Name the parasite shown.
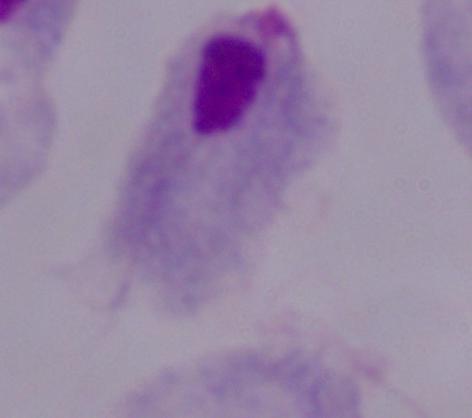

This is a trichomonad.

Photomicrograph. 1000x magnification.